Name the blood parasite species.
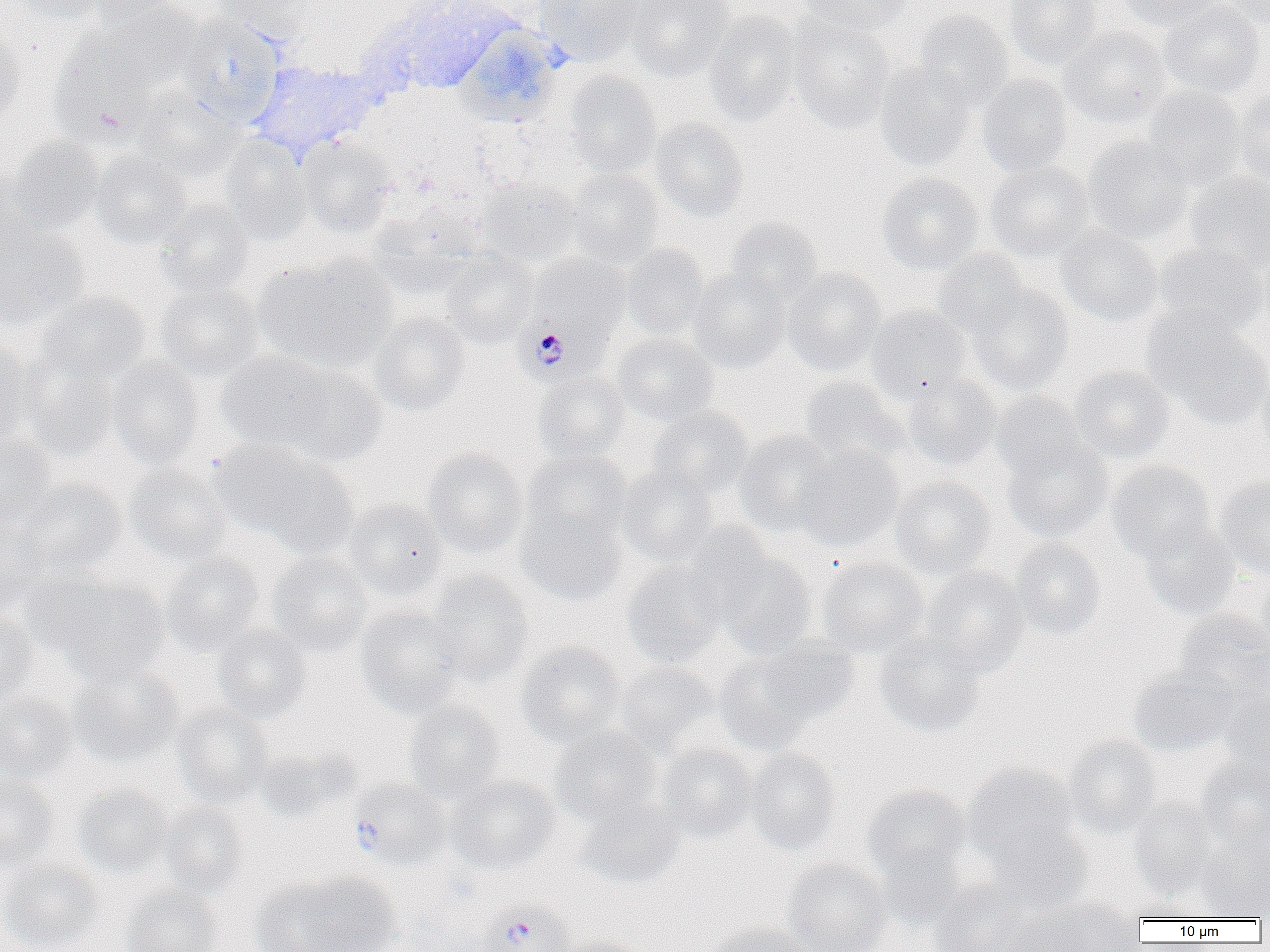
Plasmodium falciparum.

Summary:
  - Coordinate format: approximate bounding boxes as named x1/y1/x2/y2 corners in pixels
  - Uninfected red blood cell locations: (x1=2, y1=0, x2=108, y2=25), (x1=82, y1=0, x2=182, y2=27), (x1=215, y1=0, x2=316, y2=41), (x1=535, y1=0, x2=646, y2=66), (x1=626, y1=0, x2=736, y2=81), (x1=798, y1=0, x2=913, y2=34), (x1=1004, y1=0, x2=1105, y2=70), (x1=1118, y1=0, x2=1224, y2=32), (x1=1216, y1=0, x2=1270, y2=31), (x1=370, y1=1, x2=518, y2=93), (x1=1158, y1=1, x2=1266, y2=99), (x1=90, y1=3, x2=202, y2=92), (x1=912, y1=10, x2=1014, y2=110), (x1=703, y1=11, x2=802, y2=125), (x1=788, y1=15, x2=895, y2=132), (x1=178, y1=16, x2=284, y2=124), (x1=0, y1=23, x2=27, y2=131), (x1=454, y1=26, x2=561, y2=125), (x1=1058, y1=26, x2=1171, y2=129), (x1=49, y1=40, x2=155, y2=148), (x1=247, y1=59, x2=384, y2=158), (x1=874, y1=61, x2=975, y2=172), (x1=562, y1=70, x2=662, y2=176), (x1=977, y1=73, x2=1073, y2=176), (x1=1143, y1=85, x2=1248, y2=191), (x1=1234, y1=86, x2=1270, y2=188), (x1=132, y1=90, x2=242, y2=181), (x1=650, y1=118, x2=749, y2=221), (x1=1083, y1=136, x2=1193, y2=244), (x1=5, y1=137, x2=105, y2=235), (x1=298, y1=137, x2=396, y2=238), (x1=221, y1=138, x2=312, y2=244), (x1=90, y1=149, x2=192, y2=249), (x1=985, y1=161, x2=1093, y2=262), (x1=566, y1=168, x2=665, y2=266), (x1=1185, y1=171, x2=1270, y2=272), (x1=877, y1=173, x2=984, y2=275), (x1=476, y1=178, x2=582, y2=267), (x1=155, y1=199, x2=255, y2=297), (x1=368, y1=205, x2=482, y2=300), (x1=725, y1=217, x2=823, y2=303), (x1=0, y1=227, x2=88, y2=330), (x1=1057, y1=227, x2=1163, y2=327), (x1=621, y1=243, x2=709, y2=340), (x1=1153, y1=243, x2=1267, y2=339), (x1=1257, y1=243, x2=1270, y2=340), (x1=441, y1=249, x2=538, y2=347), (x1=933, y1=249, x2=1029, y2=339), (x1=253, y1=255, x2=398, y2=375), (x1=783, y1=267, x2=886, y2=375), (x1=688, y1=268, x2=790, y2=372), (x1=155, y1=278, x2=265, y2=383), (x1=968, y1=284, x2=1074, y2=396), (x1=36, y1=292, x2=151, y2=385), (x1=867, y1=304, x2=971, y2=401), (x1=370, y1=311, x2=470, y2=417), (x1=1144, y1=314, x2=1270, y2=429), (x1=613, y1=332, x2=718, y2=425), (x1=0, y1=341, x2=44, y2=446), (x1=216, y1=351, x2=334, y2=452), (x1=19, y1=355, x2=119, y2=460), (x1=106, y1=357, x2=205, y2=469), (x1=1254, y1=362, x2=1270, y2=470), (x1=278, y1=365, x2=387, y2=467), (x1=1069, y1=366, x2=1175, y2=464), (x1=532, y1=371, x2=631, y2=463), (x1=902, y1=374, x2=1002, y2=471), (x1=799, y1=377, x2=907, y2=468), (x1=991, y1=390, x2=1086, y2=481), (x1=649, y1=407, x2=753, y2=500), (x1=733, y1=430, x2=838, y2=537), (x1=0, y1=434, x2=57, y2=531), (x1=208, y1=438, x2=322, y2=538), (x1=1001, y1=438, x2=1113, y2=542), (x1=792, y1=444, x2=903, y2=551), (x1=423, y1=447, x2=527, y2=558), (x1=524, y1=450, x2=632, y2=544), (x1=255, y1=454, x2=360, y2=558), (x1=1107, y1=460, x2=1216, y2=562), (x1=124, y1=464, x2=232, y2=565), (x1=617, y1=465, x2=716, y2=566), (x1=1215, y1=474, x2=1270, y2=580), (x1=890, y1=476, x2=996, y2=578), (x1=14, y1=479, x2=126, y2=576), (x1=344, y1=499, x2=448, y2=601), (x1=517, y1=506, x2=628, y2=605), (x1=0, y1=516, x2=52, y2=614), (x1=1138, y1=520, x2=1240, y2=621), (x1=1010, y1=537, x2=1106, y2=640), (x1=712, y1=550, x2=816, y2=658), (x1=266, y1=551, x2=374, y2=655), (x1=161, y1=553, x2=264, y2=656), (x1=816, y1=556, x2=929, y2=657), (x1=622, y1=562, x2=727, y2=668), (x1=922, y1=566, x2=1029, y2=674), (x1=425, y1=569, x2=534, y2=683), (x1=1257, y1=569, x2=1270, y2=662), (x1=40, y1=577, x2=170, y2=684), (x1=0, y1=608, x2=39, y2=707), (x1=356, y1=608, x2=466, y2=717), (x1=1173, y1=609, x2=1270, y2=704), (x1=212, y1=623, x2=311, y2=723), (x1=875, y1=635, x2=986, y2=737), (x1=516, y1=640, x2=626, y2=747), (x1=754, y1=640, x2=861, y2=727), (x1=713, y1=654, x2=817, y2=755), (x1=615, y1=662, x2=717, y2=755), (x1=67, y1=663, x2=184, y2=770), (x1=1128, y1=667, x2=1237, y2=757), (x1=1222, y1=692, x2=1270, y2=779), (x1=0, y1=693, x2=78, y2=783), (x1=404, y1=700, x2=506, y2=802), (x1=173, y1=705, x2=274, y2=807), (x1=551, y1=727, x2=663, y2=826), (x1=1063, y1=735, x2=1161, y2=839), (x1=659, y1=742, x2=759, y2=843), (x1=253, y1=746, x2=356, y2=822), (x1=743, y1=747, x2=841, y2=855), (x1=1195, y1=758, x2=1270, y2=851), (x1=963, y1=762, x2=1077, y2=863), (x1=0, y1=772, x2=58, y2=871), (x1=447, y1=775, x2=559, y2=875), (x1=73, y1=785, x2=172, y2=878), (x1=862, y1=785, x2=970, y2=883), (x1=1129, y1=796, x2=1217, y2=897), (x1=575, y1=799, x2=684, y2=891), (x1=158, y1=802, x2=251, y2=897), (x1=987, y1=824, x2=1092, y2=914), (x1=1197, y1=830, x2=1270, y2=918), (x1=875, y1=845, x2=968, y2=928), (x1=0, y1=857, x2=106, y2=952), (x1=782, y1=859, x2=890, y2=952), (x1=260, y1=871, x2=401, y2=952), (x1=930, y1=879, x2=1031, y2=952), (x1=119, y1=884, x2=222, y2=952), (x1=1029, y1=896, x2=1143, y2=951), (x1=1126, y1=898, x2=1208, y2=921), (x1=1001, y1=909, x2=1100, y2=952), (x1=707, y1=922, x2=816, y2=952), (x1=553, y1=936, x2=646, y2=952)
  - Plasmodium falciparum-infected red blood cell locations: (x1=515, y1=258, x2=627, y2=384), (x1=350, y1=779, x2=451, y2=868), (x1=475, y1=900, x2=574, y2=952)
  - Image size: 1270×952 pixels
  - Magnification: 1000x
  - Modality: light microscopy
  - Preparation: thin blood film
  - Field of view: one of a larger specimen